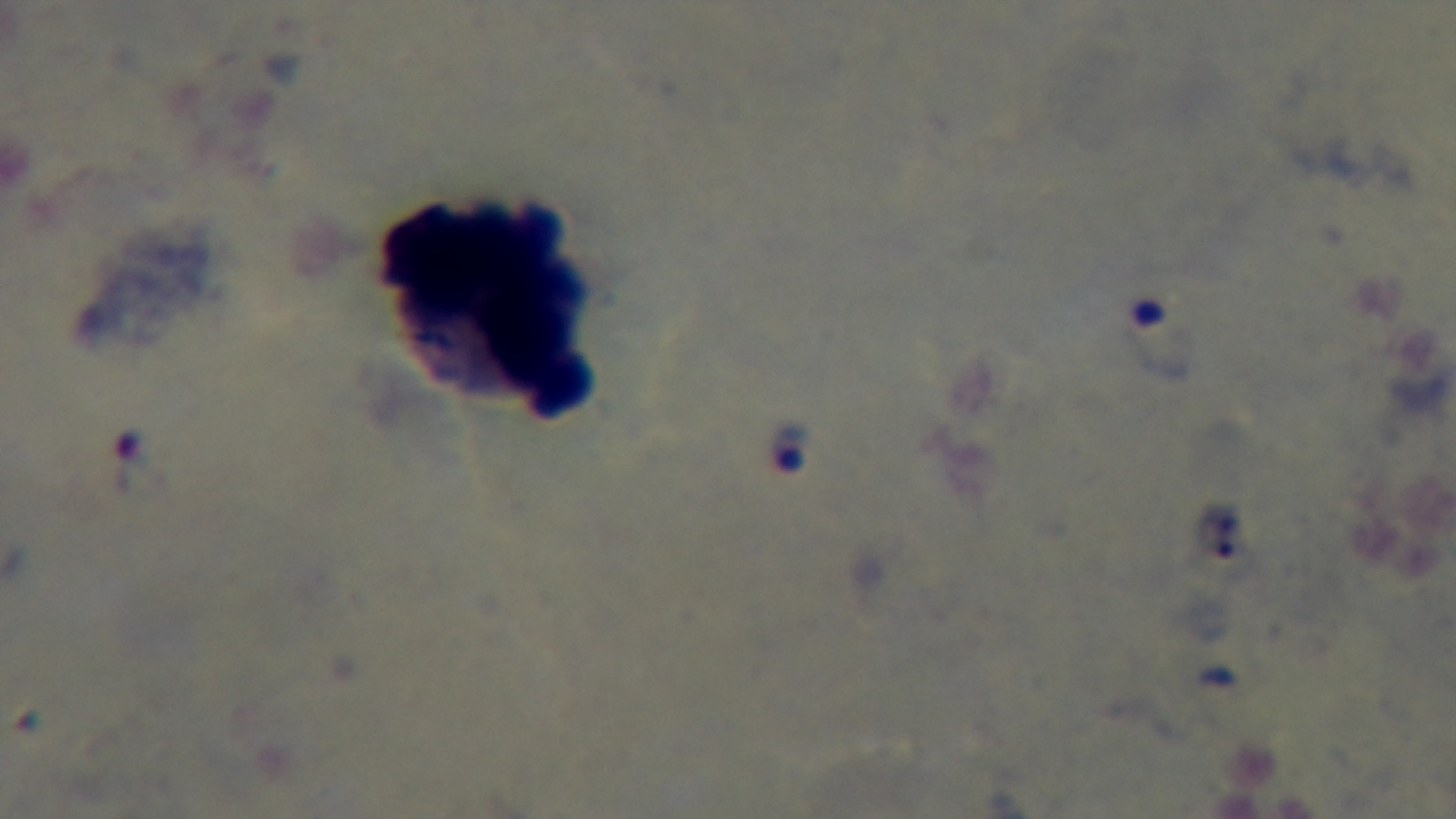
modality = light microscopy
objective = 100x oil immersion
field of view = single
stain = Giemsa
capture = mounted 4K digital camera
malaria status = infected
preparation = thick smear